Evaluate for malaria.
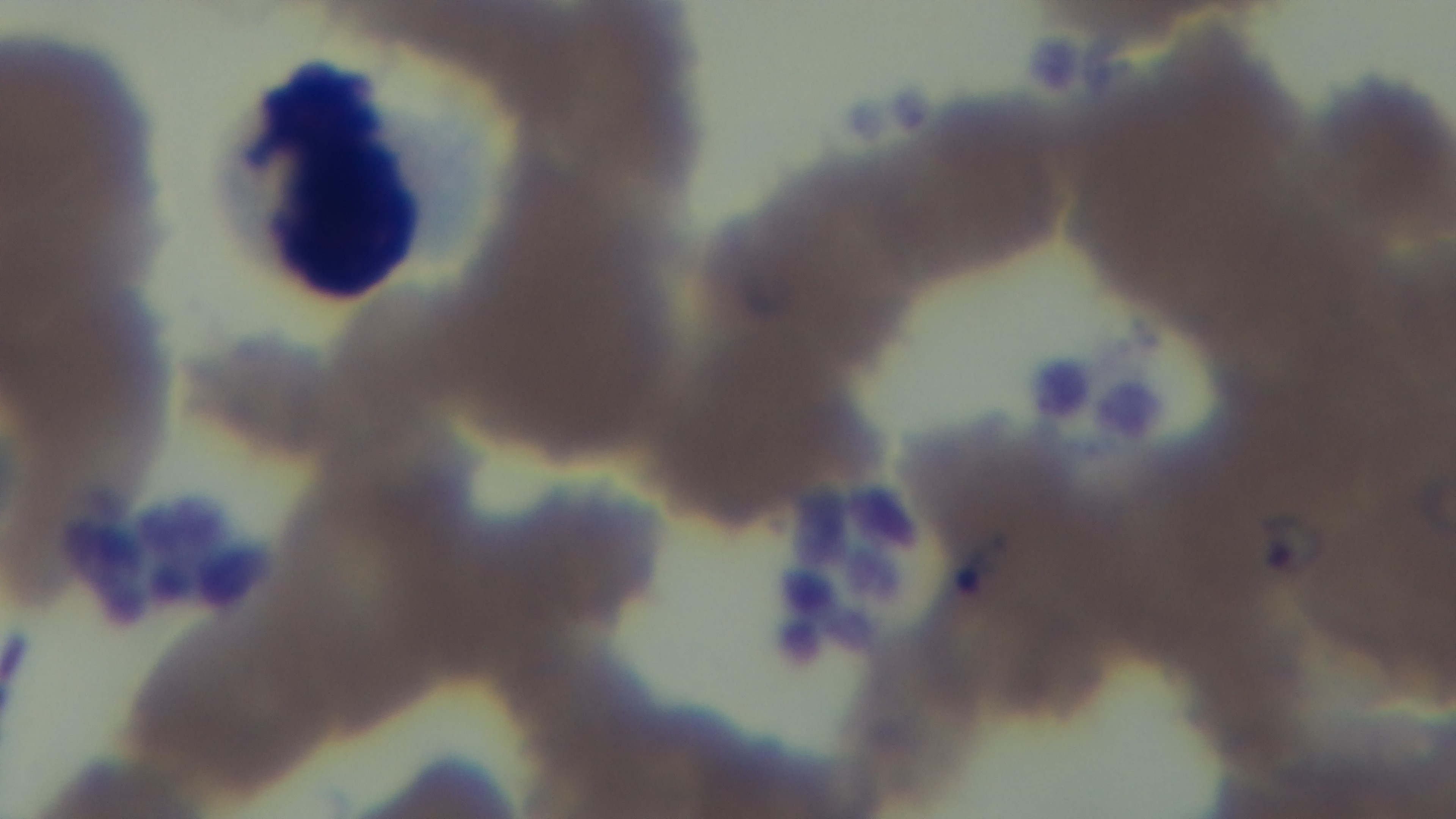

It is infected.

field of view = single
capture = mounted 4K digital camera
objective = 100x oil immersion
modality = light microscopy
stain = Giemsa
preparation = thin